Classify this cell by malaria status.
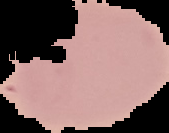

It is uninfected.

From a thin blood smear. Image is 169×133 pixels. Cell region segmented out of the field of view; the surrounding area is masked to black.